Identify the parasite.
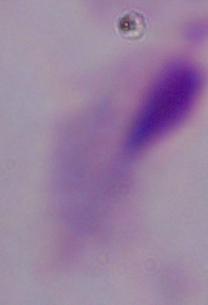
A trichomonad.

Captured at 1000x magnification. Photomicrograph.